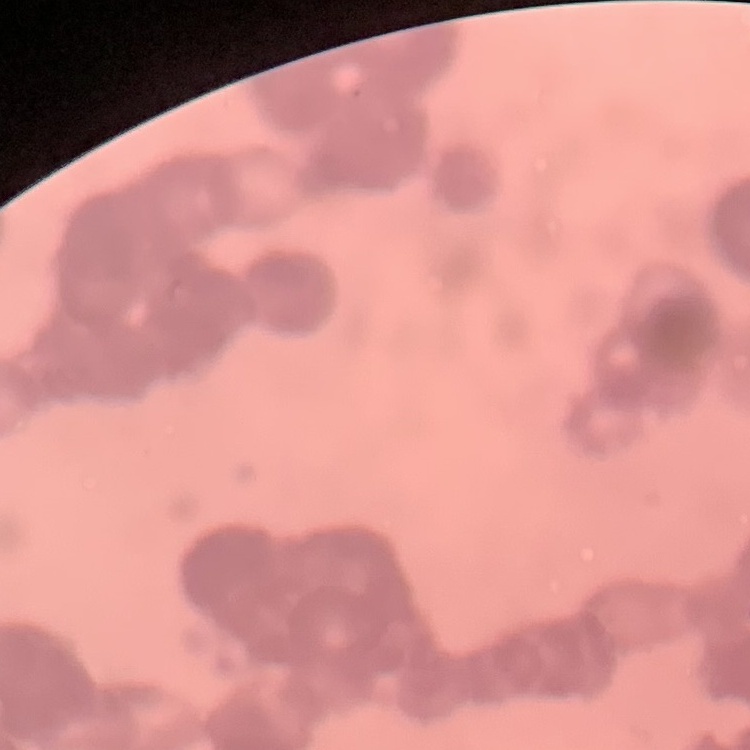

red blood cell morphology = rouleaux formation
image type = one tile cut from a larger photomicrograph
stain = Field's or Giemsa
preparation = thin peripheral smear